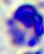

A white blood cell is seen. Micrograph. Captured at 400x magnification.